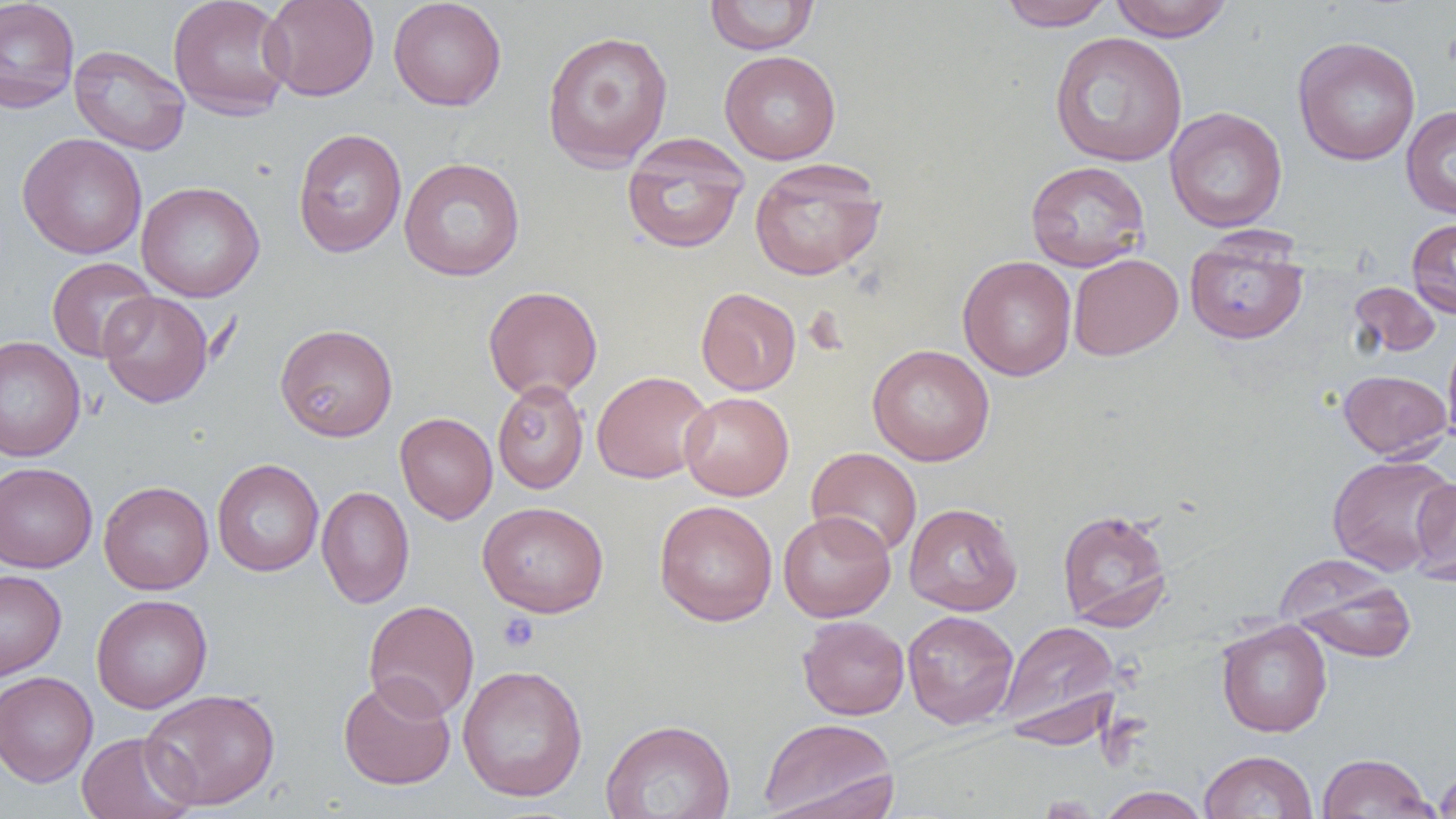 Approximate bounding boxes as named x1/y1/x2/y2 corners in pixels. Uninfected red blood cell locations: (x1=0, y1=0, x2=80, y2=114), (x1=167, y1=0, x2=294, y2=119), (x1=260, y1=0, x2=380, y2=101), (x1=388, y1=0, x2=507, y2=111), (x1=704, y1=0, x2=819, y2=55), (x1=998, y1=0, x2=1114, y2=31), (x1=1110, y1=0, x2=1234, y2=41), (x1=541, y1=29, x2=674, y2=171), (x1=1049, y1=31, x2=1188, y2=167), (x1=1292, y1=36, x2=1421, y2=166), (x1=69, y1=44, x2=191, y2=156), (x1=719, y1=50, x2=841, y2=164), (x1=1401, y1=106, x2=1456, y2=218), (x1=1165, y1=107, x2=1288, y2=233), (x1=292, y1=128, x2=407, y2=257), (x1=17, y1=133, x2=147, y2=259), (x1=622, y1=134, x2=749, y2=254), (x1=399, y1=157, x2=526, y2=281), (x1=748, y1=158, x2=887, y2=281), (x1=1025, y1=161, x2=1150, y2=271), (x1=136, y1=181, x2=265, y2=302), (x1=1406, y1=218, x2=1456, y2=318), (x1=1184, y1=230, x2=1308, y2=345), (x1=1068, y1=253, x2=1182, y2=361), (x1=958, y1=255, x2=1077, y2=381), (x1=46, y1=257, x2=159, y2=363), (x1=1349, y1=281, x2=1441, y2=358), (x1=483, y1=285, x2=603, y2=402), (x1=696, y1=287, x2=802, y2=396), (x1=98, y1=291, x2=214, y2=408), (x1=275, y1=323, x2=398, y2=441), (x1=1442, y1=330, x2=1456, y2=451), (x1=0, y1=334, x2=86, y2=462), (x1=867, y1=344, x2=995, y2=466), (x1=1338, y1=369, x2=1452, y2=460), (x1=592, y1=370, x2=713, y2=483), (x1=492, y1=379, x2=589, y2=494), (x1=680, y1=391, x2=793, y2=500), (x1=395, y1=412, x2=498, y2=524), (x1=806, y1=447, x2=922, y2=558), (x1=1327, y1=454, x2=1455, y2=575), (x1=212, y1=459, x2=324, y2=576), (x1=0, y1=462, x2=98, y2=573), (x1=1410, y1=476, x2=1456, y2=586), (x1=99, y1=480, x2=214, y2=594), (x1=316, y1=485, x2=414, y2=608), (x1=654, y1=500, x2=778, y2=626), (x1=478, y1=501, x2=609, y2=617), (x1=904, y1=502, x2=1022, y2=615), (x1=1057, y1=508, x2=1173, y2=631), (x1=778, y1=510, x2=895, y2=622), (x1=1281, y1=563, x2=1418, y2=662), (x1=0, y1=569, x2=66, y2=681), (x1=91, y1=594, x2=212, y2=713), (x1=363, y1=599, x2=480, y2=721), (x1=902, y1=610, x2=1019, y2=729), (x1=797, y1=615, x2=910, y2=720), (x1=1216, y1=619, x2=1332, y2=737), (x1=997, y1=620, x2=1121, y2=743), (x1=457, y1=664, x2=588, y2=802), (x1=0, y1=671, x2=98, y2=787), (x1=338, y1=675, x2=456, y2=790), (x1=141, y1=688, x2=281, y2=810), (x1=758, y1=716, x2=898, y2=819), (x1=600, y1=718, x2=737, y2=819), (x1=76, y1=731, x2=197, y2=819), (x1=1199, y1=750, x2=1318, y2=819), (x1=1316, y1=752, x2=1437, y2=818), (x1=1434, y1=766, x2=1456, y2=818), (x1=1096, y1=787, x2=1211, y2=819). Platelet locations: (x1=498, y1=611, x2=539, y2=652). Slide-level diagnosis: no evidence of blood parasites. Thin blood smear. One field of a larger specimen. Optical microscopy. Image is 1456×819 pixels. Captured at 1000x magnification.